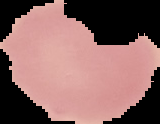

Summary:
  - Preparation: thin blood smear
  - Image size: 160×124 pixels
  - Malaria status: uninfected
  - Image type: cell region segmented out of the field of view; surrounding area masked to black